Comment on the morphology of the red blood cells.
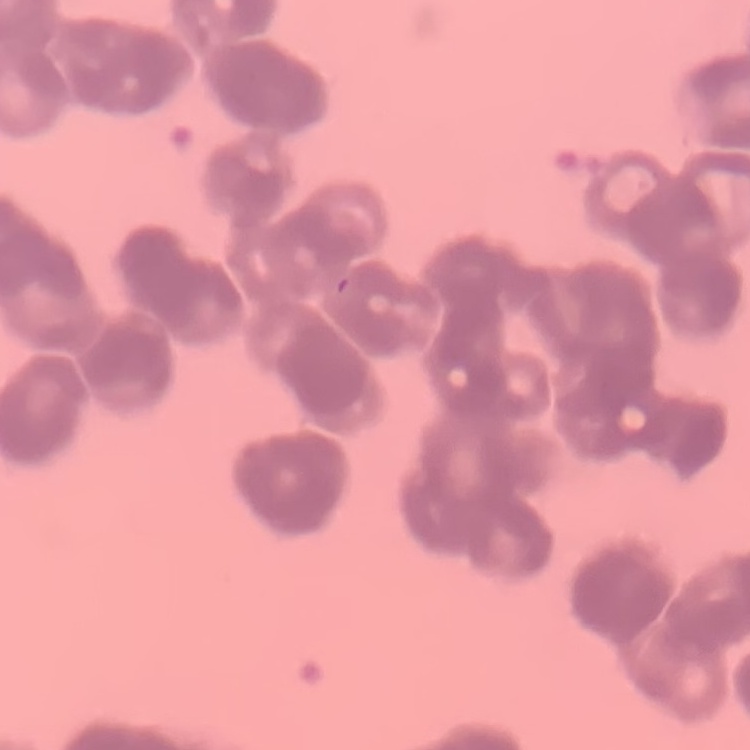
Rouleaux formation.

stain = Field's or Giemsa
image type = square crop of a larger photomicrograph
preparation = thin blood smear